Report the malaria status of this cell.
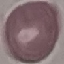
Uninfected.

Summary:
  - Capture: smartphone camera at the microscope eyepiece
  - Stain: Giemsa
  - Image type: cell patch, automatically extracted from a larger field of view and resized to 64 × 64 pixels
  - Preparation: thin blood smear